Classify this cell by malaria status.
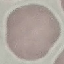

Uninfected.

Giemsa stain. Automatically extracted cell patch, resized to 64 × 64 pixels. Photographed with a smartphone camera at the microscope eyepiece. Thin blood smear.